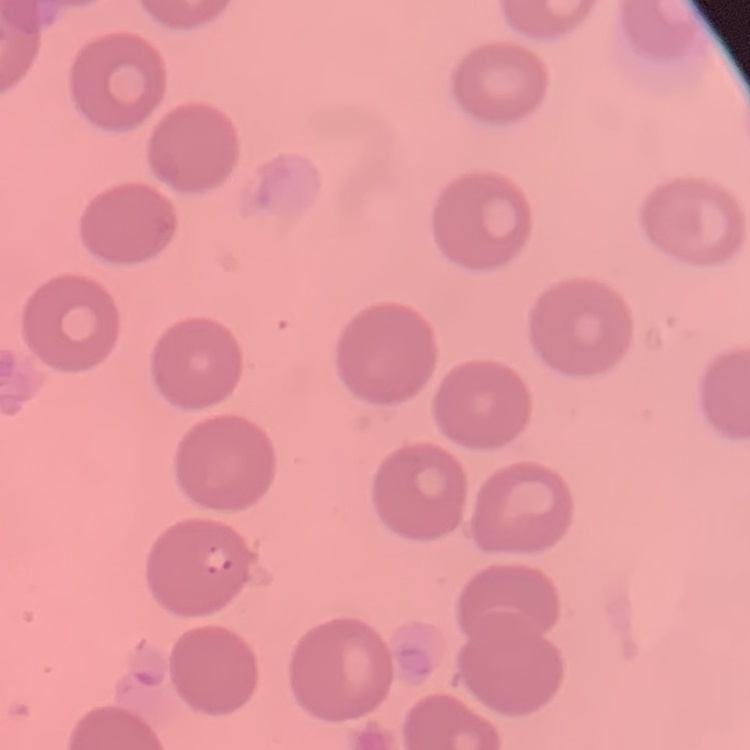 The erythrocytes show no rouleaux formation. Field's or Giemsa stain. Square crop of a larger photomicrograph. Thin peripheral smear.